Assess this cell for malaria.
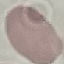
It is uninfected.

image type = automatically extracted cell patch, resized to 64 × 64 pixels
preparation = thin smear
stain = Giemsa
capture = smartphone camera at the microscope eyepiece